Outline each Plasmodium ovale-infected red blood cell.
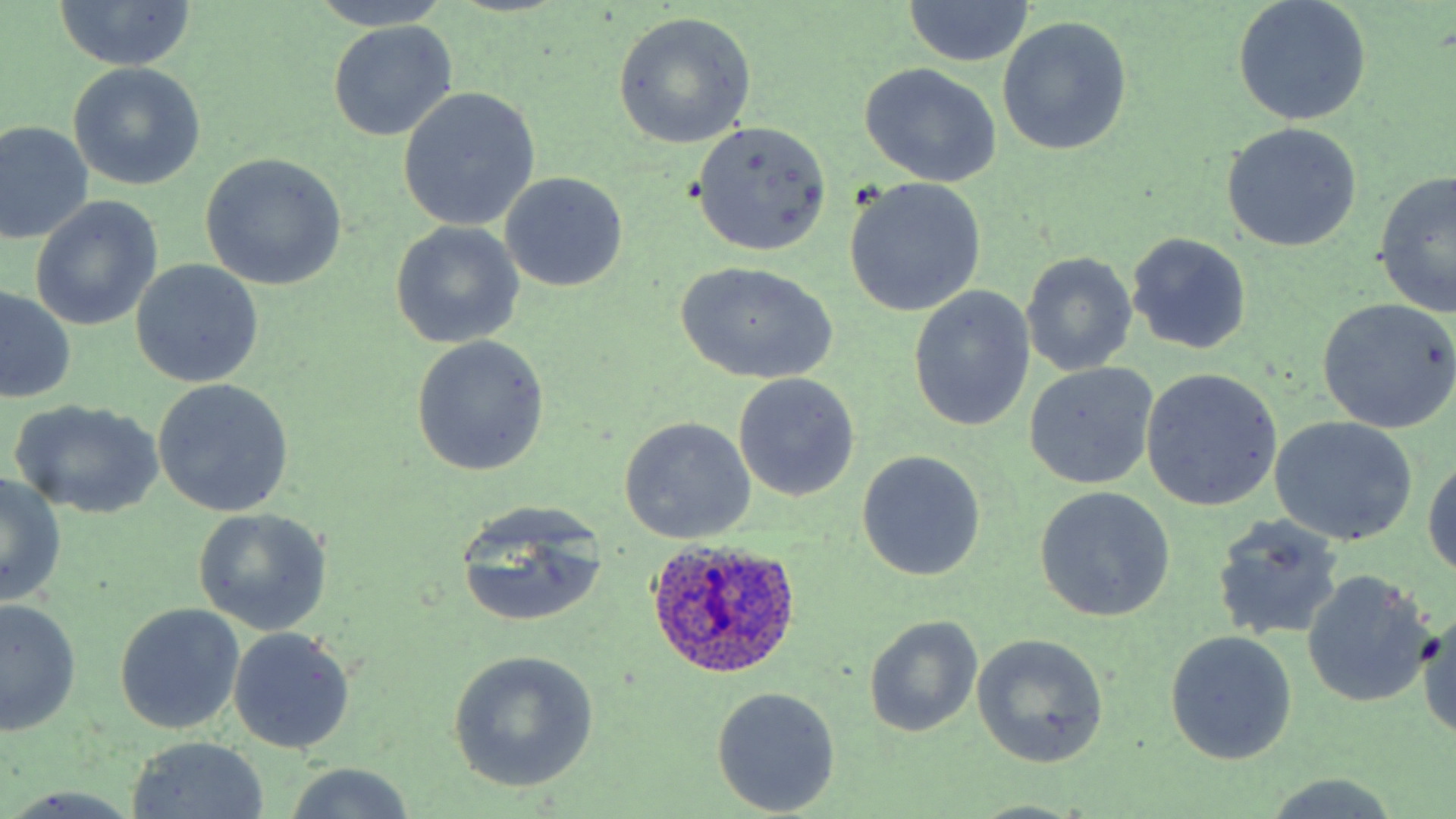

Approximate bounding boxes as (x1,y1)-(x2,y2) corner pairs in pixels.
Plasmodium ovale-infected red blood cells: (645,534)-(803,681).

Uninfected red blood cell locations: (307,0)-(458,32), (901,1)-(1035,67), (1233,1)-(1372,126), (49,2)-(200,72), (612,12)-(756,149), (996,17)-(1132,156), (327,22)-(458,141), (67,62)-(206,191), (859,63)-(1002,188), (397,87)-(541,232), (689,120)-(834,255), (0,121)-(93,246), (1220,123)-(1362,251), (199,153)-(347,291), (501,172)-(629,292), (1375,172)-(1456,318), (844,178)-(986,317), (30,196)-(163,331), (390,222)-(525,348), (1126,232)-(1252,354), (1021,252)-(1137,377), (130,259)-(264,388), (675,262)-(838,385), (908,286)-(1035,433), (0,288)-(77,406), (1317,299)-(1456,434), (409,336)-(549,477), (1024,366)-(1158,489), (1139,369)-(1282,510), (732,373)-(860,503), (151,379)-(295,517), (9,400)-(163,519), (618,416)-(756,544), (1268,416)-(1416,545), (856,451)-(986,581), (1424,460)-(1456,583), (1,473)-(66,607), (1033,485)-(1175,620), (453,504)-(610,631), (193,508)-(332,635), (1210,514)-(1344,644), (1301,571)-(1436,708), (1,596)-(80,734), (115,603)-(245,735), (1418,609)-(1456,741), (864,616)-(982,738), (228,627)-(354,754), (1164,630)-(1297,765), (972,633)-(1109,768), (445,648)-(598,794), (711,687)-(842,815), (126,737)-(271,818), (282,764)-(417,819), (1260,775)-(1405,817), (2,788)-(146,819), (968,800)-(1088,817). Slide-level diagnosis: Plasmodium ovale. Captured at 1000x magnification. Image is 1456×819 pixels. One field of a larger specimen. Thin blood film. May-Grünwald-Giemsa-stained preparation. Optical microscopy.